Classify this cell by malaria status.
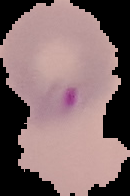

It is parasitized.

preparation: thin blood smear
image_size: 130×196 pixels
image_type: segmented cell region on a black background